Assess this cell for malaria.
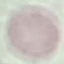

Uninfected.

Giemsa stain. Photographed with a smartphone camera at the microscope eyepiece. Automatically extracted cell patch, resized to 64 × 64 pixels. Thin blood smear.